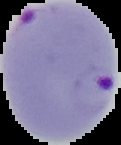
{
  "image_size": "121×145 pixels",
  "preparation": "thin blood smear",
  "malaria_status": "parasitized",
  "image_type": "segmented cell region with the area outside set to black"
}